Report the malaria status of this cell.
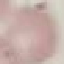
Uninfected.

preparation: thin smear
image_type: automatically extracted cell patch, resized to 64 × 64 pixels
capture: smartphone through the microscope eyepiece
stain: Giemsa